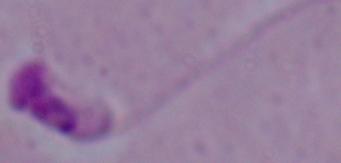
identification: Leishmania
modality: photomicrograph
magnification: 1000x